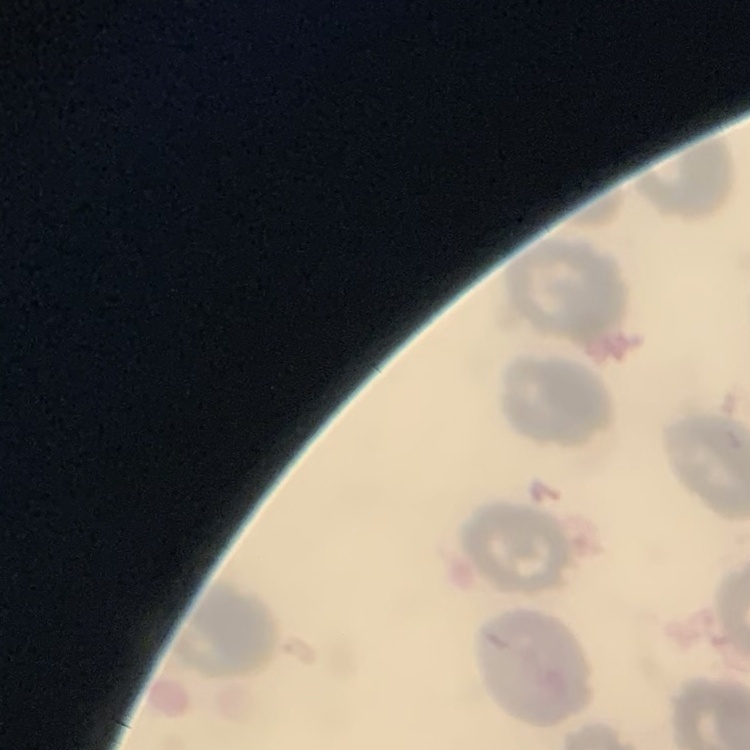 The erythrocytes exhibit no rouleaux formation. One tile cut from a larger photomicrograph. Thin blood smear. Stained with either Field's or Giemsa.